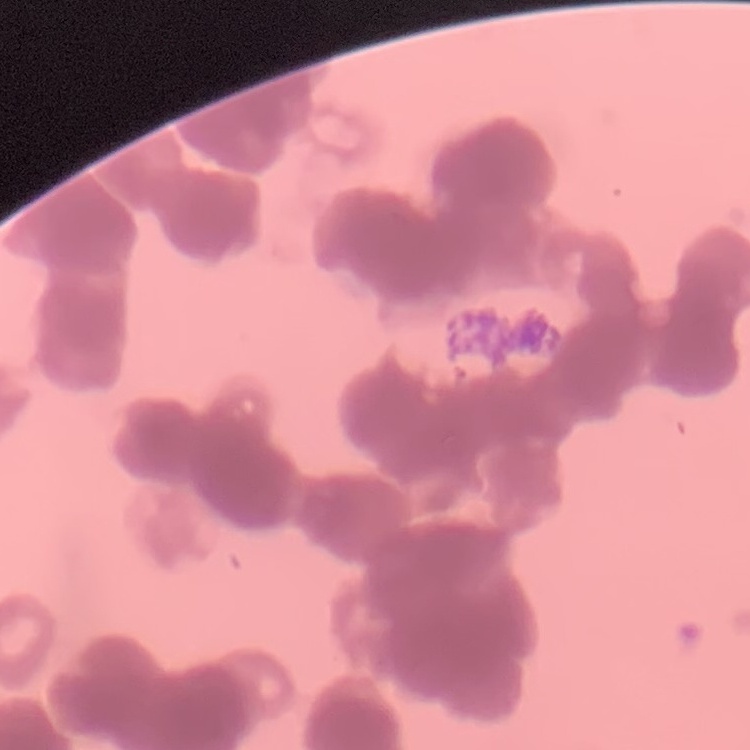
erythrocyte morphology = rouleaux formation
stain = Field's or Giemsa
preparation = thin blood film
image type = one tile cut from a larger photomicrograph